Name the parasite shown.
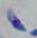
This is Toxoplasma gondii.

Micrograph. 1000x magnification.